Identify the parasite.
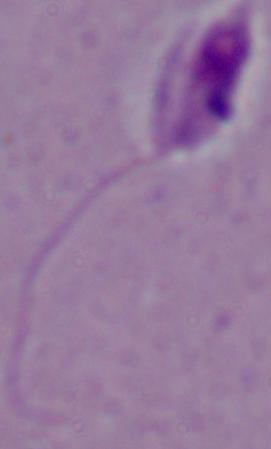
This is Leishmania.

Summary:
  - Modality: photomicrograph
  - Magnification: 1000x